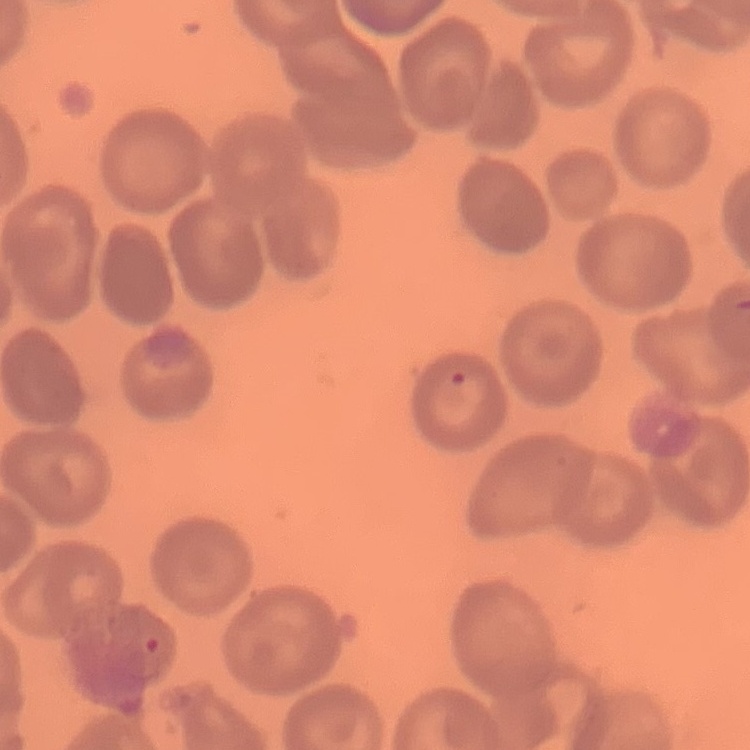
red blood cell morphology = no rouleaux formation
image type = square crop of a larger photomicrograph
preparation = thin blood smear
stain = Field's or Giemsa